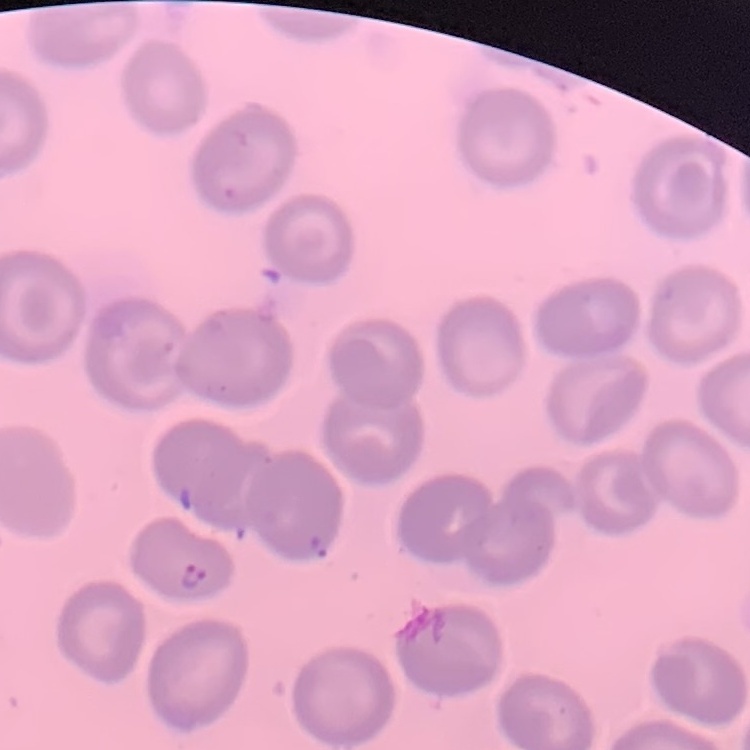

The erythrocytes show no rouleaux formation. Stained with either Field's or Giemsa. One tile cut from a larger photomicrograph. Thin blood film.